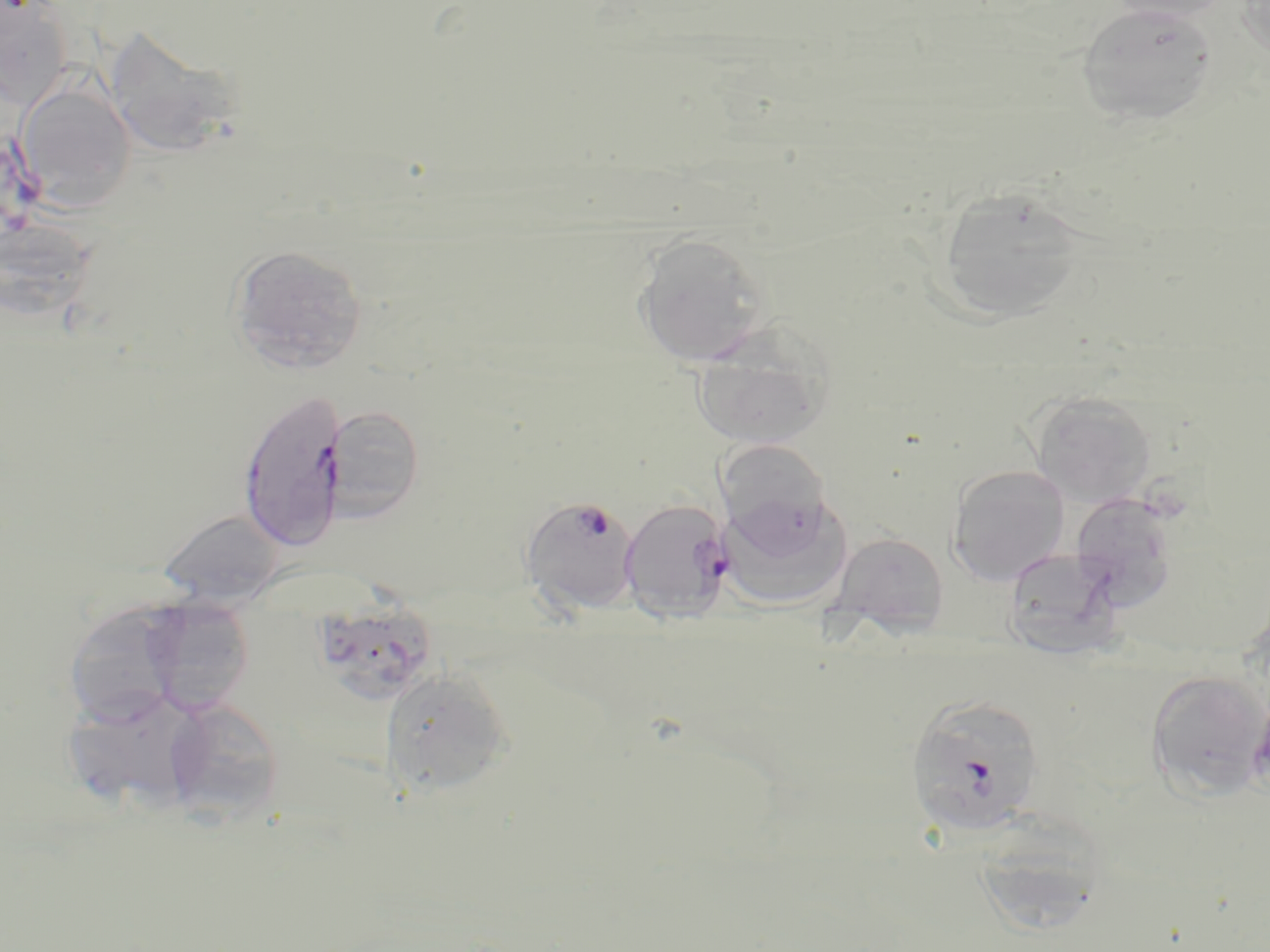

Approximate bounding boxes as named x1/y1/x2/y2 corners in pixels. Plasmodium falciparum-infected red blood cell locations: (x1=236, y1=389, x2=348, y2=551), (x1=520, y1=495, x2=641, y2=614), (x1=619, y1=497, x2=734, y2=623), (x1=905, y1=693, x2=1048, y2=839). Uninfected red blood cell locations: (x1=1105, y1=0, x2=1232, y2=23), (x1=1237, y1=1, x2=1270, y2=65), (x1=1, y1=3, x2=74, y2=108), (x1=1075, y1=3, x2=1219, y2=127), (x1=110, y1=37, x2=243, y2=153), (x1=15, y1=80, x2=137, y2=213), (x1=932, y1=184, x2=1089, y2=326), (x1=632, y1=233, x2=771, y2=367), (x1=228, y1=243, x2=368, y2=374), (x1=689, y1=321, x2=836, y2=450), (x1=1029, y1=391, x2=1156, y2=507), (x1=324, y1=404, x2=425, y2=522), (x1=714, y1=440, x2=836, y2=551), (x1=948, y1=464, x2=1070, y2=585), (x1=718, y1=492, x2=851, y2=608), (x1=1068, y1=493, x2=1179, y2=611), (x1=158, y1=509, x2=286, y2=608), (x1=830, y1=531, x2=949, y2=638), (x1=1001, y1=546, x2=1126, y2=657), (x1=150, y1=592, x2=255, y2=718), (x1=317, y1=598, x2=445, y2=704), (x1=68, y1=605, x2=186, y2=727), (x1=380, y1=666, x2=514, y2=799), (x1=1145, y1=670, x2=1269, y2=801), (x1=65, y1=689, x2=211, y2=822), (x1=162, y1=698, x2=285, y2=825), (x1=974, y1=806, x2=1105, y2=929). Slide-level diagnosis: Plasmodium falciparum. Light microscopy. 1000x magnification. Image is 1270×952 pixels. May-Grünwald-Giemsa stain. Thin blood film. Single field of view.